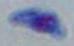

Toxoplasma gondii is seen. Micrograph. Captured at 1000x magnification.